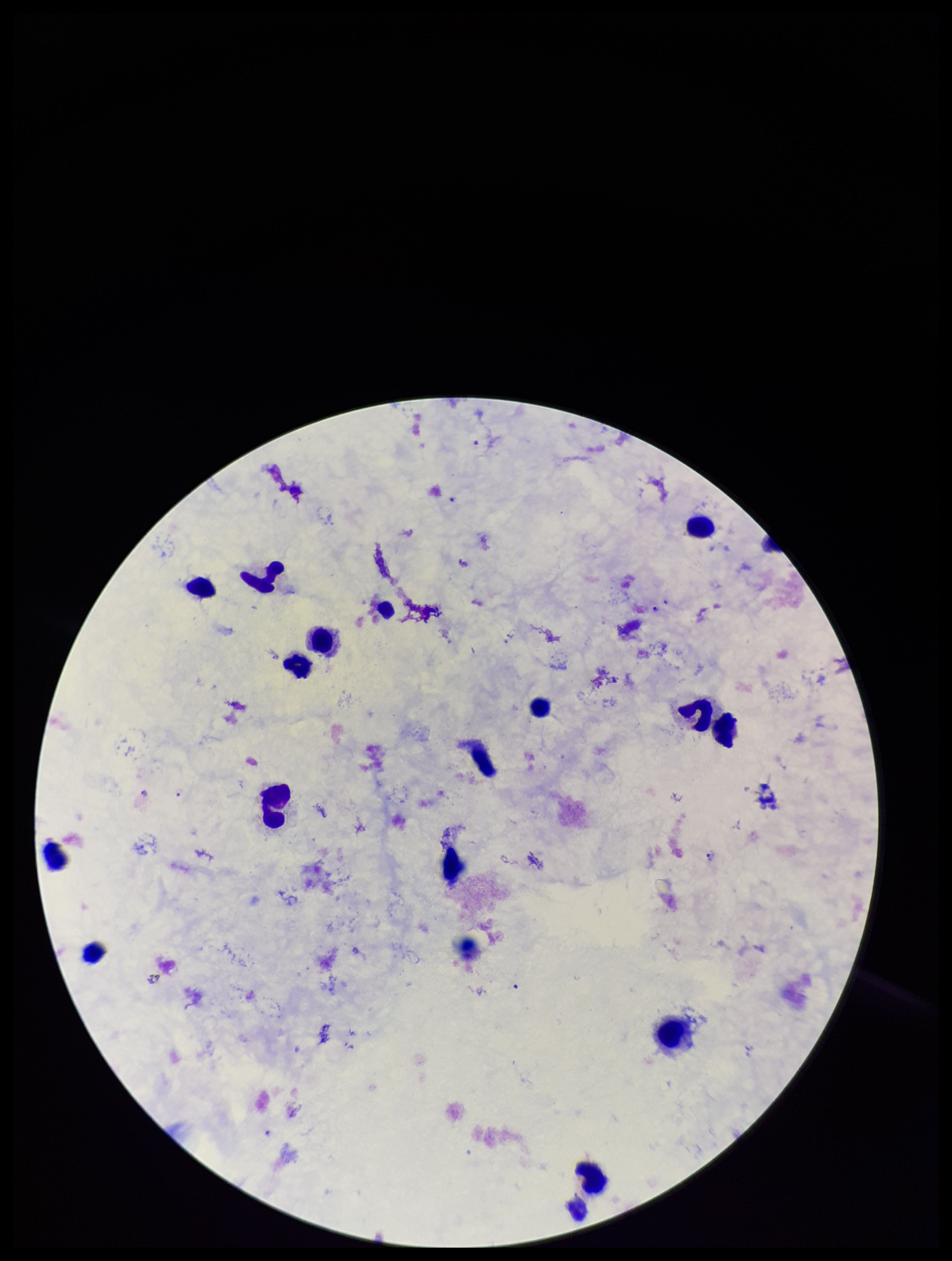
Parasite count: 3. Image is 952×1261 pixels. Preparation: thick smear. Plasmodium parasites: seen. Species reported for this patient: Plasmodium falciparum. Leukocyte count: 16. Single field of view. Stained with Giemsa. Smartphone photograph taken through the eyepiece of a microscope. Patient malaria status: positive.